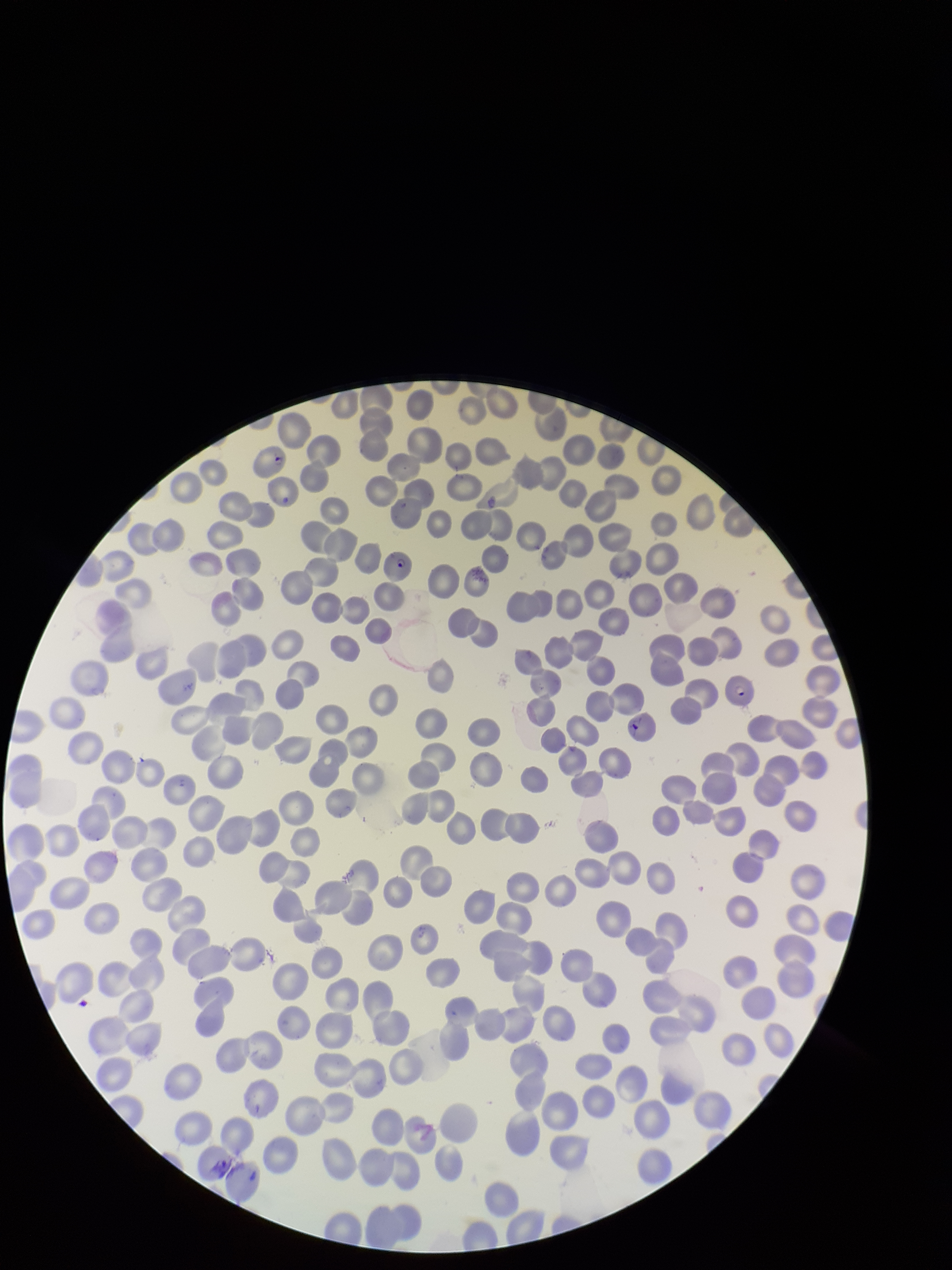
Summary:
  - Patient malaria status: infected
  - Image size: 952×1270 pixels
  - Parasitized red blood cell count: 4
  - Stain: Giemsa
  - Species reported for this patient: Plasmodium falciparum
  - Field of view: one from this slide
  - Red blood cell count: 254
  - Capture: smartphone photograph through the microscope eyepiece
  - Parasitized red blood cells: detected
  - Preparation: thin blood smear